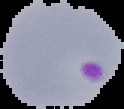

{
  "image_size": "124×109 pixels",
  "preparation": "thin blood smear",
  "image_type": "segmented cell region on a black background",
  "result": "malaria parasites detected"
}